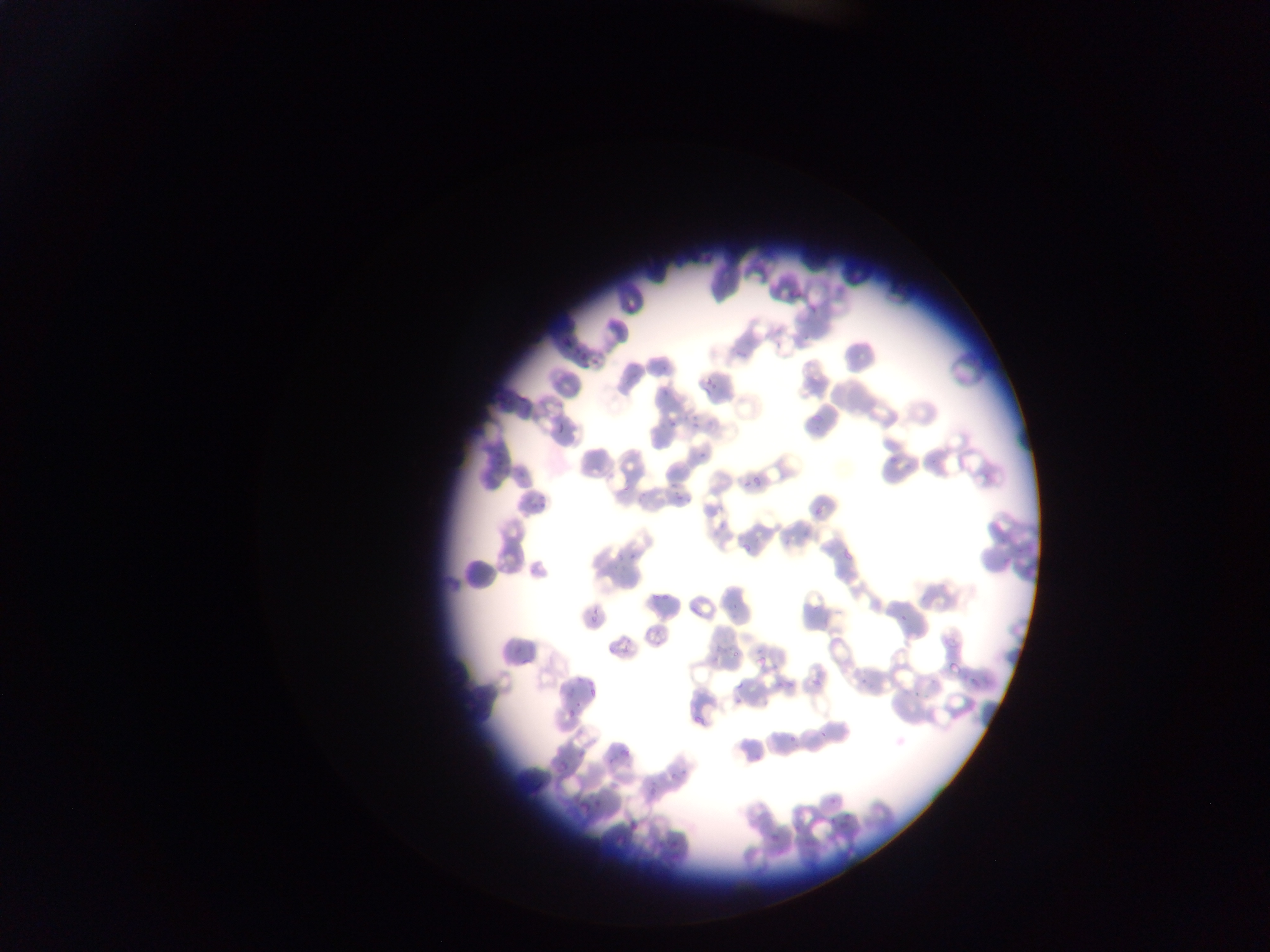
image size = 1270×952 pixels
capture = mobile-phone photograph through a microscope
country = Ghana
field of view = single
malaria parasite locations = approximate bounding boxes as (left, top, right, bottom) in pixels: (786, 284, 801, 301), (808, 301, 817, 317), (561, 332, 579, 354), (571, 342, 589, 361), (733, 349, 747, 364), (583, 354, 601, 369), (702, 376, 720, 393), (659, 379, 677, 396), (502, 385, 527, 410), (520, 402, 531, 422), (690, 403, 707, 426), (808, 409, 823, 426), (666, 411, 680, 428), (556, 420, 566, 434), (700, 442, 711, 459), (491, 449, 505, 469), (886, 453, 897, 466), (515, 465, 528, 486), (984, 466, 996, 479), (744, 473, 766, 490), (666, 477, 684, 500), (619, 479, 631, 495), (637, 488, 649, 504), (524, 489, 550, 509), (672, 492, 686, 509), (812, 501, 830, 516), (717, 515, 731, 534), (794, 530, 812, 539), (739, 539, 756, 567), (627, 545, 642, 562), (843, 550, 852, 559), (613, 551, 625, 563), (997, 558, 1012, 567), (650, 583, 669, 602), (730, 601, 745, 612), (588, 610, 599, 626), (897, 611, 911, 622), (943, 626, 961, 647), (512, 636, 526, 657), (605, 640, 628, 660), (732, 647, 742, 658), (754, 652, 769, 670), (711, 656, 721, 666), (947, 660, 960, 676), (572, 668, 581, 687), (776, 668, 798, 691), (813, 672, 824, 687), (969, 675, 983, 690), (859, 678, 867, 688), (733, 680, 744, 693), (586, 684, 597, 698), (907, 687, 923, 700), (736, 696, 747, 706), (574, 699, 584, 714), (564, 709, 578, 720), (694, 715, 707, 728), (780, 716, 801, 748), (818, 726, 832, 740), (620, 740, 634, 761), (555, 752, 577, 774), (751, 752, 765, 767), (600, 753, 615, 768), (666, 761, 682, 788), (645, 782, 658, 799), (590, 786, 612, 810), (573, 794, 592, 813), (828, 795, 837, 804), (824, 811, 843, 834), (837, 813, 854, 830), (625, 817, 640, 832), (789, 819, 800, 833), (765, 829, 783, 843), (654, 840, 667, 851), (673, 848, 680, 864) | approximate (x, y) pixel centers of objects too small to bound: (816, 427)
preparation = thin blood film